Outline platelets.
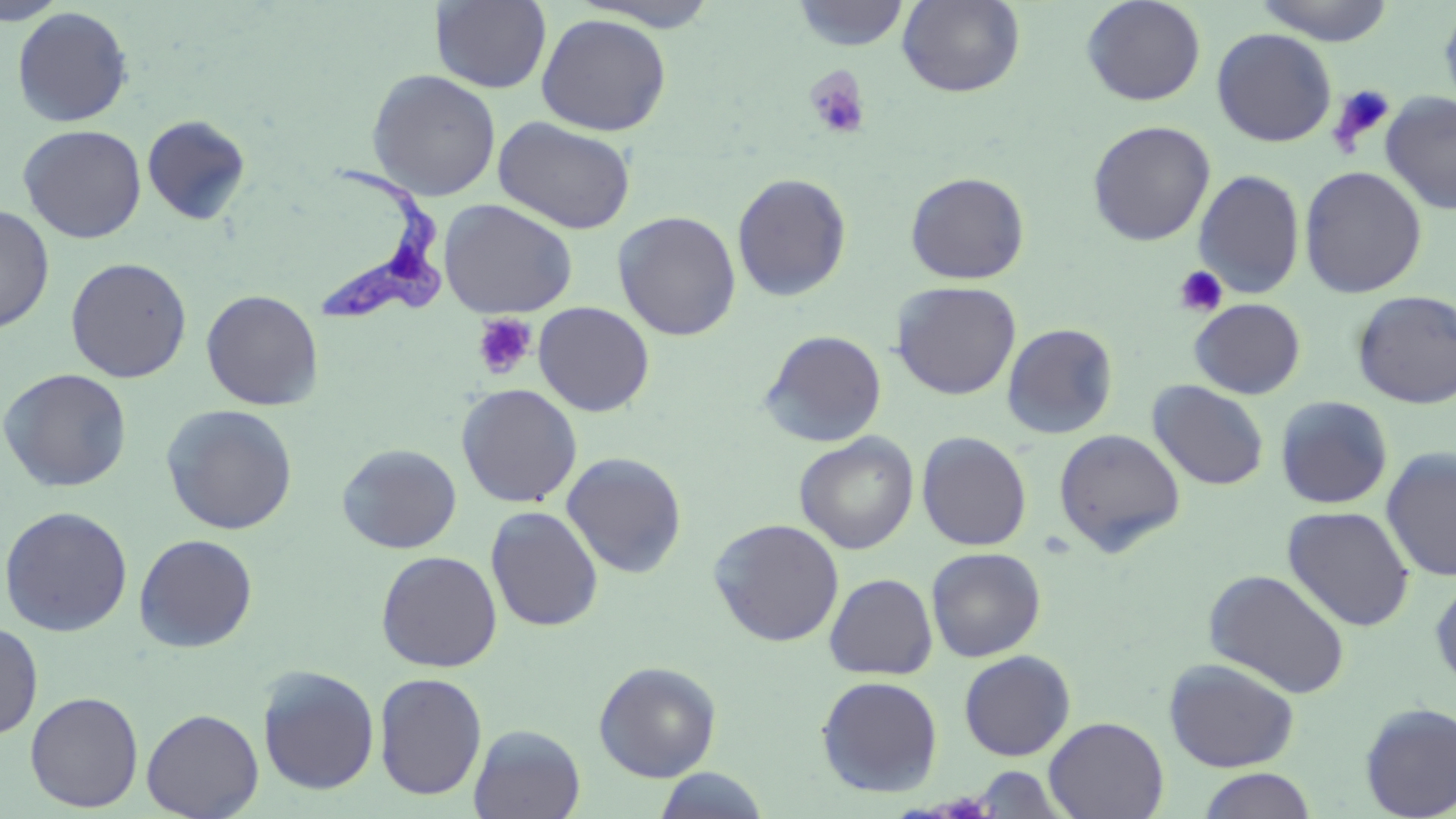
Approximate bounding boxes as named x1/y1/x2/y2 corners in pixels.
Platelets: (x1=804, y1=67, x2=872, y2=141), (x1=1329, y1=84, x2=1397, y2=155), (x1=1173, y1=265, x2=1229, y2=317), (x1=472, y1=313, x2=537, y2=379).

{
  "slide_level_diagnosis": "Trypanosoma brucei",
  "field_of_view": "single",
  "image_size": "1456×819 pixels",
  "stain": "May-Grünwald-Giemsa",
  "magnification": "1000x",
  "trypanosoma_brucei_locations": "approximate bounding boxes as named x1/y1/x2/y2 corners in pixels: (x1=308, y1=150, x2=452, y2=323)",
  "uninfected_red_blood_cell_locations": "approximate bounding boxes as named x1/y1/x2/y2 corners in pixels: (x1=1, y1=0, x2=68, y2=26), (x1=431, y1=0, x2=552, y2=94), (x1=897, y1=0, x2=1025, y2=97), (x1=1080, y1=0, x2=1207, y2=106), (x1=1253, y1=0, x2=1395, y2=45), (x1=571, y1=1, x2=724, y2=31), (x1=791, y1=1, x2=910, y2=51), (x1=1439, y1=1, x2=1456, y2=119), (x1=11, y1=6, x2=133, y2=127), (x1=535, y1=13, x2=672, y2=136), (x1=1211, y1=27, x2=1337, y2=147), (x1=366, y1=69, x2=502, y2=201), (x1=1380, y1=90, x2=1455, y2=216), (x1=142, y1=114, x2=250, y2=225), (x1=493, y1=116, x2=636, y2=235), (x1=1087, y1=120, x2=1215, y2=246), (x1=18, y1=124, x2=146, y2=244), (x1=1299, y1=165, x2=1427, y2=298), (x1=1192, y1=169, x2=1306, y2=299), (x1=905, y1=171, x2=1029, y2=284), (x1=731, y1=172, x2=852, y2=302), (x1=438, y1=198, x2=578, y2=319), (x1=0, y1=204, x2=55, y2=334), (x1=612, y1=211, x2=741, y2=340), (x1=65, y1=257, x2=192, y2=383), (x1=891, y1=281, x2=1022, y2=400), (x1=201, y1=289, x2=324, y2=410), (x1=1352, y1=290, x2=1455, y2=409), (x1=1189, y1=298, x2=1306, y2=399), (x1=533, y1=301, x2=655, y2=417), (x1=1002, y1=322, x2=1119, y2=439), (x1=759, y1=330, x2=887, y2=448), (x1=0, y1=368, x2=133, y2=493), (x1=1147, y1=380, x2=1269, y2=491), (x1=456, y1=383, x2=582, y2=508), (x1=1274, y1=396, x2=1393, y2=509), (x1=161, y1=404, x2=298, y2=535), (x1=1053, y1=428, x2=1186, y2=557), (x1=916, y1=431, x2=1033, y2=551), (x1=794, y1=432, x2=919, y2=554), (x1=337, y1=443, x2=461, y2=554), (x1=1381, y1=447, x2=1456, y2=582), (x1=561, y1=452, x2=687, y2=579), (x1=0, y1=505, x2=133, y2=637), (x1=1282, y1=505, x2=1415, y2=631), (x1=485, y1=506, x2=604, y2=632), (x1=708, y1=518, x2=844, y2=647), (x1=134, y1=533, x2=258, y2=652), (x1=926, y1=546, x2=1046, y2=662), (x1=376, y1=550, x2=502, y2=672), (x1=1204, y1=568, x2=1351, y2=699), (x1=824, y1=573, x2=938, y2=679), (x1=1429, y1=574, x2=1456, y2=695), (x1=0, y1=620, x2=43, y2=739), (x1=958, y1=650, x2=1076, y2=761), (x1=1163, y1=658, x2=1300, y2=772), (x1=593, y1=660, x2=721, y2=782), (x1=257, y1=665, x2=380, y2=796), (x1=374, y1=672, x2=488, y2=800), (x1=816, y1=675, x2=943, y2=798), (x1=25, y1=691, x2=144, y2=812), (x1=1358, y1=701, x2=1456, y2=819), (x1=141, y1=708, x2=264, y2=819), (x1=1044, y1=716, x2=1169, y2=819), (x1=469, y1=724, x2=586, y2=819), (x1=969, y1=765, x2=1070, y2=817), (x1=653, y1=767, x2=771, y2=819), (x1=1196, y1=768, x2=1319, y2=819)",
  "modality": "optical microscopy",
  "preparation": "thin blood film"
}